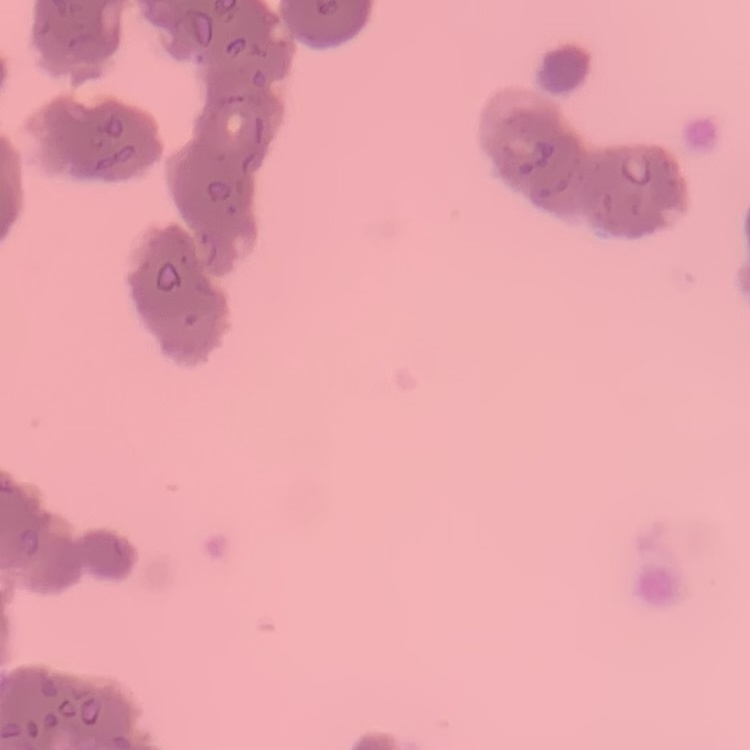
The red blood cells show rouleaux formation. Field's or Giemsa stain. Thin blood smear. One tile cut from a larger photomicrograph.